Name the parasite shown.
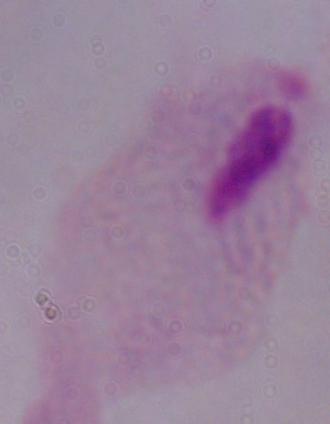

This is a trichomonad.

Photomicrograph. Captured at 1000x magnification.